State which cell type is depicted.
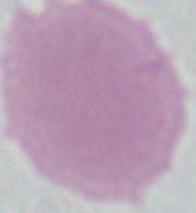

An erythrocyte.

Summary:
  - Magnification: 1000x
  - Modality: micrograph